Assess this cell for malaria.
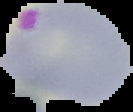
It is parasitized.

Cell region segmented out of the field of view; the surrounding area is masked to black. From a thin blood film. Image is 133×112 pixels.